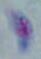
Micrograph. 1000x magnification. Toxoplasma gondii is seen.